Classify this cell by malaria status.
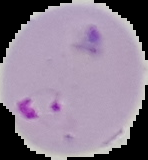

It is parasitized.

preparation: thin blood smear
image_size: 148×160 pixels
image_type: cell region segmented out of the field of view; surrounding area masked to black